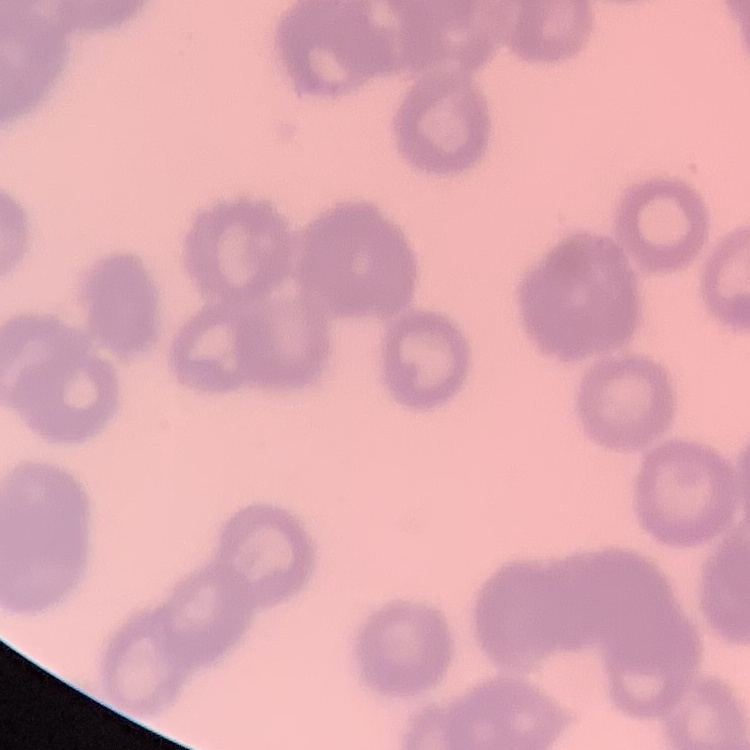

erythrocyte morphology = rouleaux formation
stain = Field's or Giemsa
image type = one tile cut from a larger photomicrograph
preparation = thin blood film